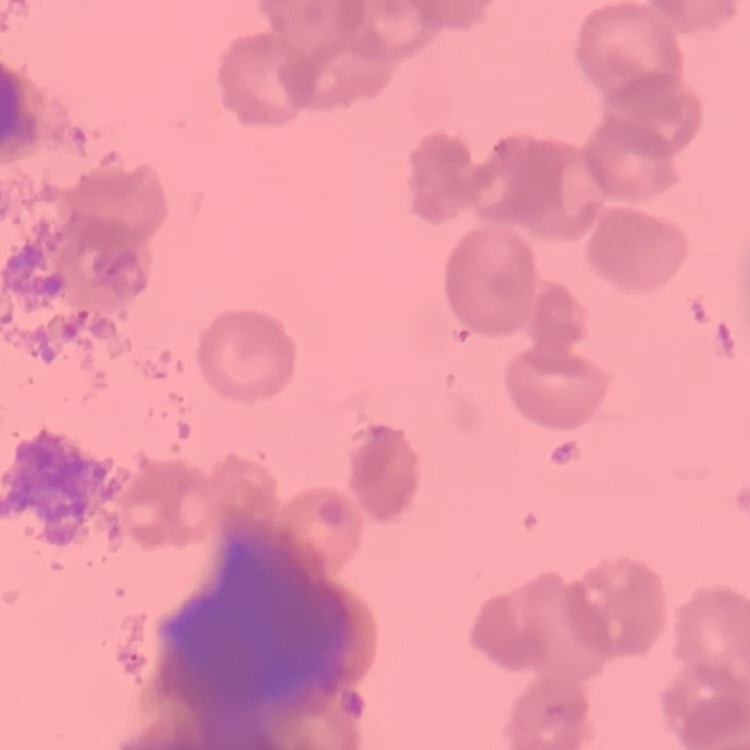
Summary:
  - Red blood cell morphology: rouleaux formation
  - Preparation: thin peripheral smear
  - Stain: Field's or Giemsa
  - Image type: square crop of a larger photomicrograph